Assess this cell for malaria.
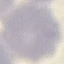
It is uninfected.

capture = smartphone camera at the microscope eyepiece
preparation = thin smear
image type = automatically extracted cell patch, resized to 64 × 64 pixels
stain = Giemsa